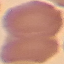
Summary:
  - Malaria status: uninfected
  - Stain: Giemsa
  - Image type: automatically extracted cell patch, resized to 64 × 64 pixels
  - Capture: smartphone through the microscope eyepiece
  - Preparation: thin blood smear